State the preparation type.
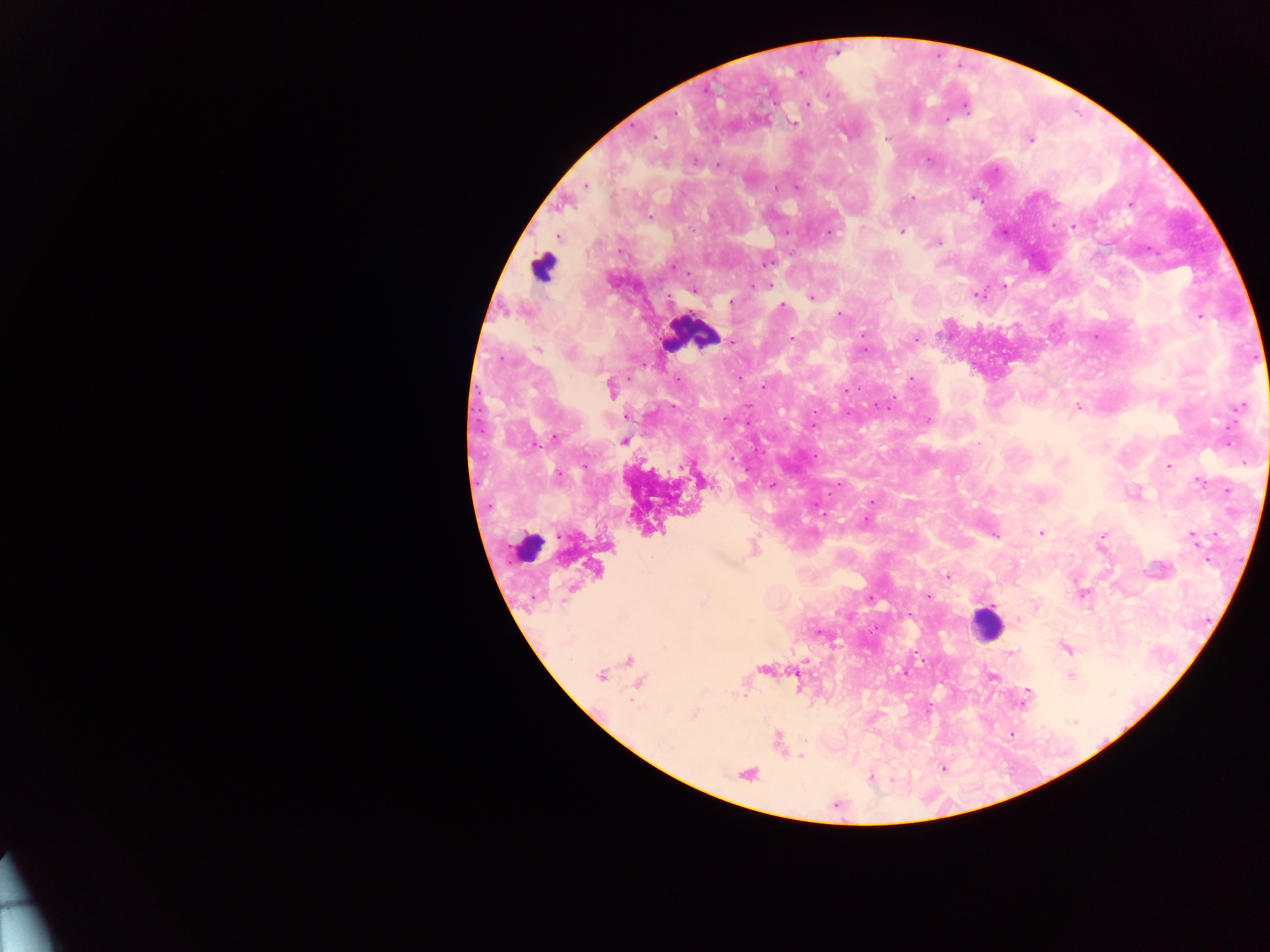
Thick blood smear.

Approximate centers as {x, y} in pixels. Leukocyte locations: {542, 267}, {690, 334}, {662, 495}, {527, 548}, {986, 624}. Plasmodium parasite locations: {836, 51}, {799, 72}, {827, 94}, {808, 105}, {964, 106}, {791, 121}, {654, 137}, {887, 138}, {1029, 140}, {717, 165}, {585, 185}, {795, 186}, {912, 198}, {1130, 203}, {649, 216}, {1075, 226}, {901, 232}, {828, 233}, {558, 235}, {938, 241}, {1146, 248}, {767, 261}, {672, 266}, {767, 284}, {1004, 285}, {693, 290}, {977, 295}, {810, 296}, {731, 301}, {782, 307}, {838, 313}, {1199, 315}, {862, 335}, {916, 338}, {791, 339}, {732, 342}, {538, 349}, {739, 377}, {910, 379}, {763, 386}, {611, 388}, {844, 391}, {1239, 406}, {1077, 407}, {628, 416}, {928, 420}, {554, 437}, {623, 440}, {979, 442}, {1226, 442}, {1169, 465}, {1200, 481}, {772, 485}, {1227, 490}, {871, 501}, {865, 521}, {1041, 533}, {994, 535}, {1192, 536}, {1102, 537}, {753, 548}, {594, 569}, {948, 576}, {1082, 594}, {926, 596}, {818, 632}, {1065, 647}, {1011, 655}, {630, 661}, {764, 669}, {904, 672}, {601, 675}, {991, 675}, {1070, 676}, {638, 682}, {1026, 692}, {1024, 698}, {693, 713}, {1011, 734}, {800, 756}, {943, 768}, {746, 773}, {870, 777}. Image is 1270×952 pixels. One field of view. Collected in Ghana. Photographed through a microscope with a mobile-phone camera.